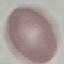

Summary:
  - Result: negative for malaria parasites
  - Preparation: thin blood film
  - Image type: automatically extracted cell patch, resized to 64 × 64 pixels
  - Stain: Giemsa
  - Capture: smartphone camera at the microscope eyepiece